Describe the morphology of the red blood cells.
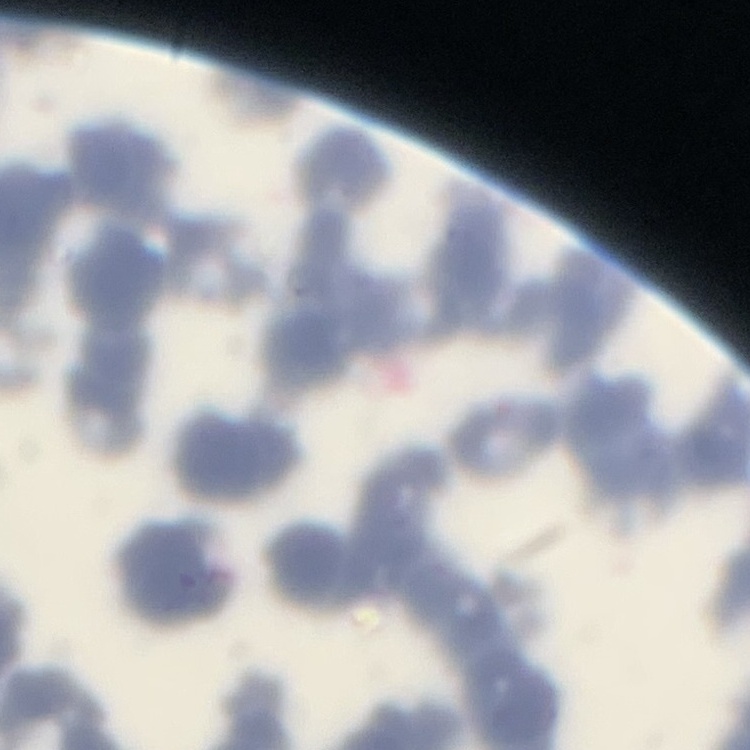
They show rouleaux formation.

image_type: one tile cut from a larger photomicrograph
stain: Field's or Giemsa
preparation: thin blood smear